Assess this cell for malaria.
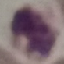

It is uninfected.

Giemsa-stained preparation. Thin blood film. Photographed with a smartphone camera at the microscope eyepiece. Automatically extracted cell patch, resized to 64 × 64 pixels.